Assess this cell for malaria.
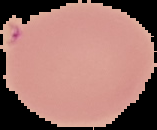

It is uninfected.

preparation = thin blood smear
image size = 157×130 pixels
image type = cell region segmented out of the field of view; surrounding area masked to black